Report the malaria status of this cell.
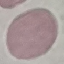

Uninfected.

Summary:
  - Preparation: thin blood film
  - Image type: automatically extracted cell patch, resized to 64 × 64 pixels
  - Stain: Giemsa
  - Capture: smartphone through the microscope eyepiece